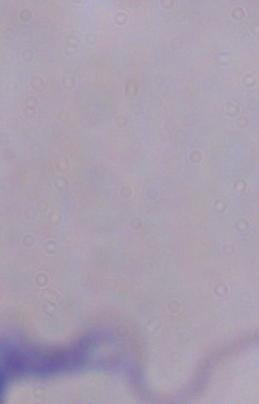 A trypanosome is seen. Captured at 1000x magnification. Micrograph.